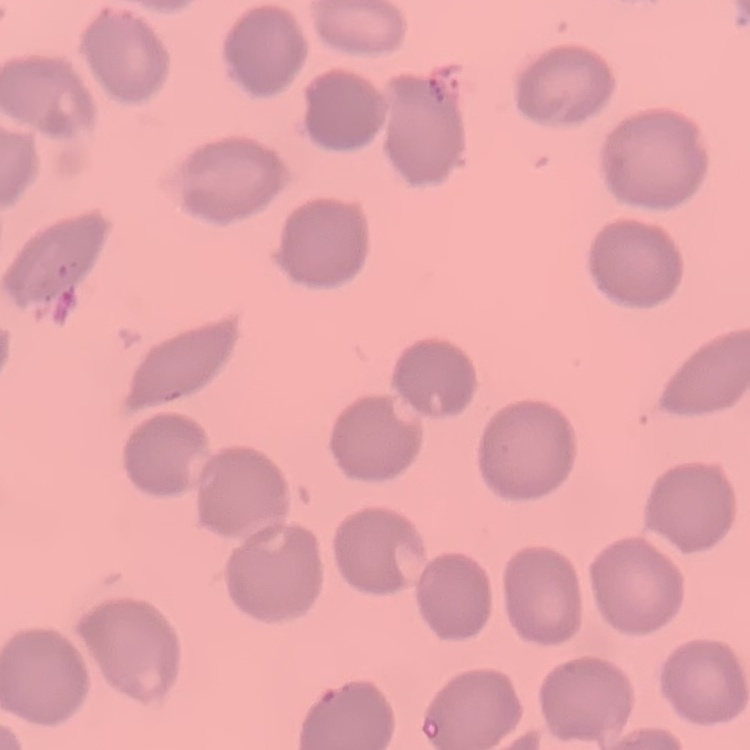

{
  "red_blood_cell_morphology": "no rouleaux formation",
  "stain": "Field's or Giemsa",
  "preparation": "thin peripheral smear",
  "image_type": "one tile cut from a larger photomicrograph"
}